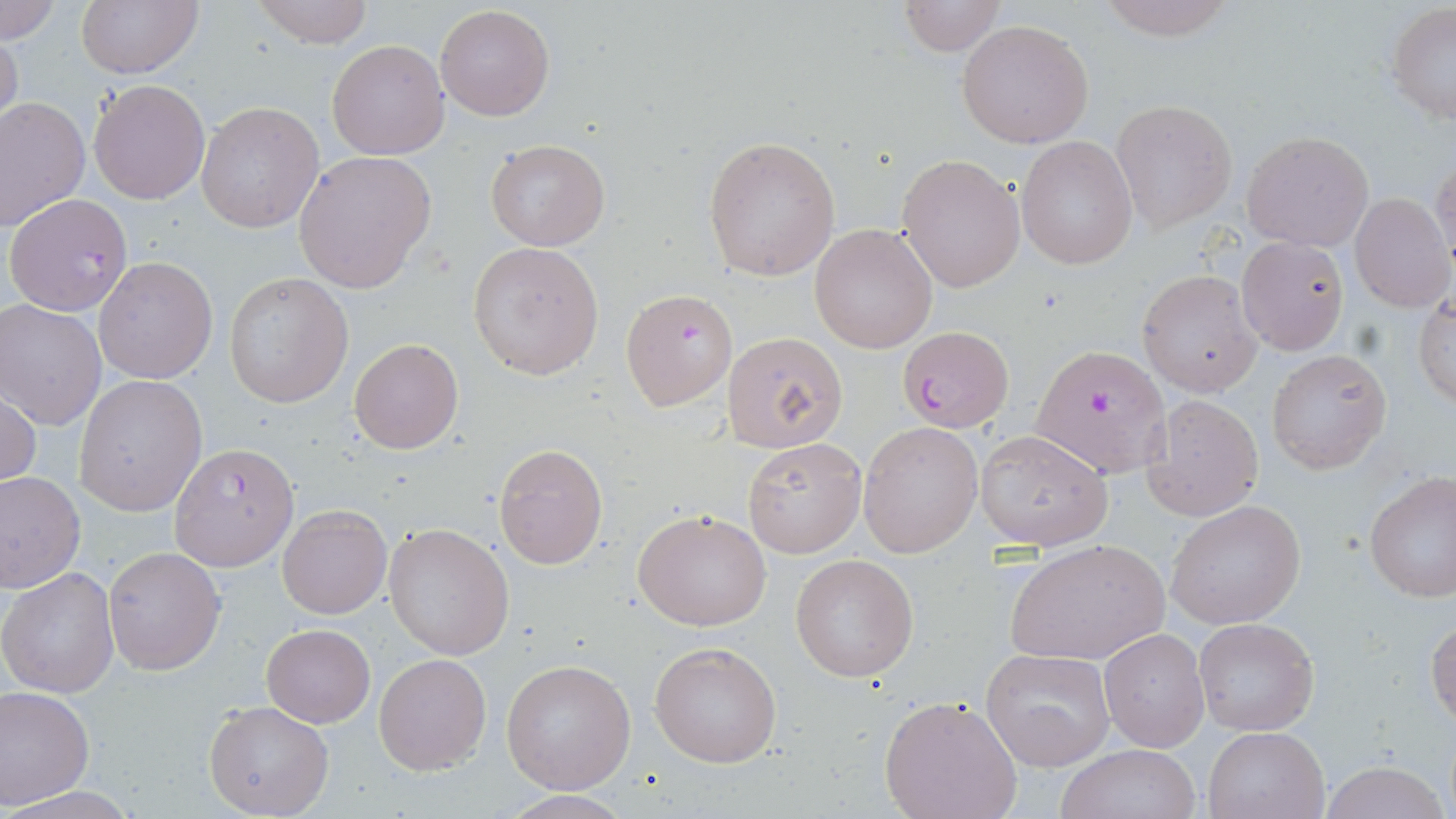

Plasmodium falciparum-infected red blood cell locations = approximate bounding boxes as (x1,y1)-(x2,y2) corner pairs in pixels: (5,192)-(133,317), (619,287)-(737,410), (898,328)-(1013,432), (1032,346)-(1169,477), (168,442)-(299,571)
slide-level diagnosis = Plasmodium falciparum
uninfected red blood cell locations = approximate bounding boxes as (x1,y1)-(x2,y2) corner pairs in pixels: (74,0)-(204,78), (247,0)-(375,47), (1090,0)-(1242,43), (0,1)-(61,43), (894,2)-(1009,55), (435,4)-(555,121), (1387,4)-(1456,126), (957,19)-(1094,149), (0,27)-(23,136), (327,40)-(449,159), (89,78)-(210,205), (0,96)-(90,231), (1111,99)-(1237,232), (195,100)-(325,233), (1241,130)-(1374,251), (703,136)-(841,280), (1017,136)-(1138,269), (485,138)-(609,251), (293,150)-(438,293), (897,153)-(1025,293), (1430,153)-(1455,271), (1349,192)-(1455,312), (810,223)-(939,354), (1235,235)-(1348,355), (468,242)-(604,380), (86,254)-(211,383), (1139,268)-(1263,396), (225,274)-(351,408), (1415,290)-(1455,410), (1,299)-(109,431), (724,331)-(847,451), (348,337)-(464,455), (1267,348)-(1391,472), (73,374)-(206,516), (0,382)-(40,492), (1143,394)-(1264,519), (858,422)-(983,557), (976,429)-(1113,551), (742,436)-(866,557), (494,444)-(608,569), (1363,471)-(1456,606), (0,472)-(85,592), (1167,500)-(1304,630), (277,502)-(392,619), (632,506)-(771,631), (383,523)-(513,660), (1006,537)-(1168,666), (104,547)-(225,675), (790,553)-(920,682), (1,567)-(118,698), (1426,616)-(1456,727), (1193,617)-(1321,737), (260,622)-(376,728), (1099,626)-(1211,753), (649,641)-(782,768), (981,648)-(1114,770), (373,652)-(491,775), (501,659)-(637,793), (0,686)-(94,809), (878,695)-(1022,819), (204,701)-(331,818), (1203,725)-(1329,818), (1055,743)-(1203,819), (1320,761)-(1449,819)
field of view = single
stain = May-Grünwald-Giemsa
magnification = 1000x
image size = 1456×819 pixels
preparation = thin blood smear
modality = optical microscopy